Point out each malaria parasite.
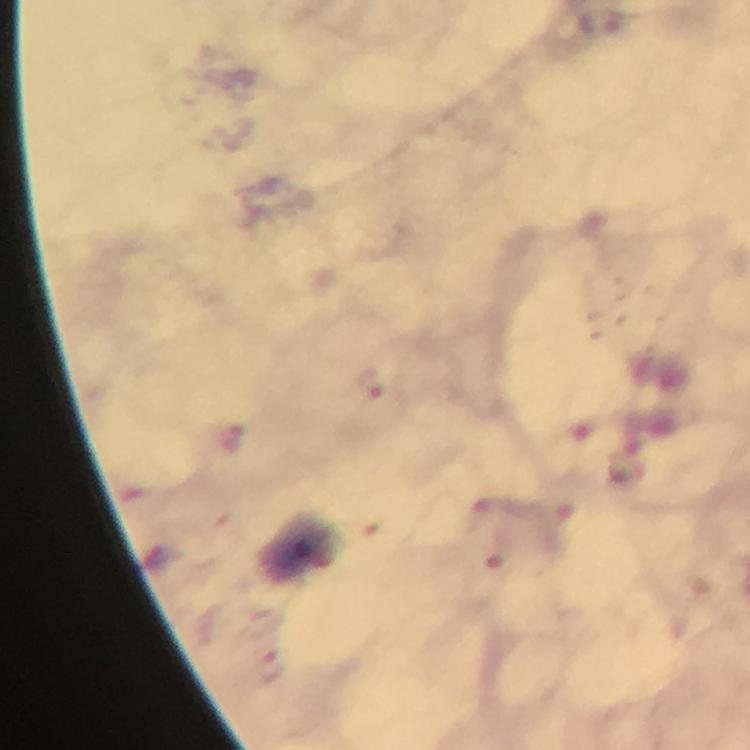

Approximate centers as (x, y) in pixels.
Malaria parasites: (366, 383), (268, 666).

preparation = thick blood smear
image size = 750×750 pixels
magnification = 100x
cropped from = a single field of view
immersion oil = applied
stain = Giemsa
context = from a diagnostic examination for malaria
capture = smartphone mounted on the microscope